Assess this cell for malaria.
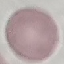

It is uninfected.

{
  "image_type": "automatically extracted cell patch, resized to 64 × 64 pixels",
  "preparation": "thin blood film",
  "capture": "smartphone camera at the microscope eyepiece",
  "stain": "Giemsa"
}